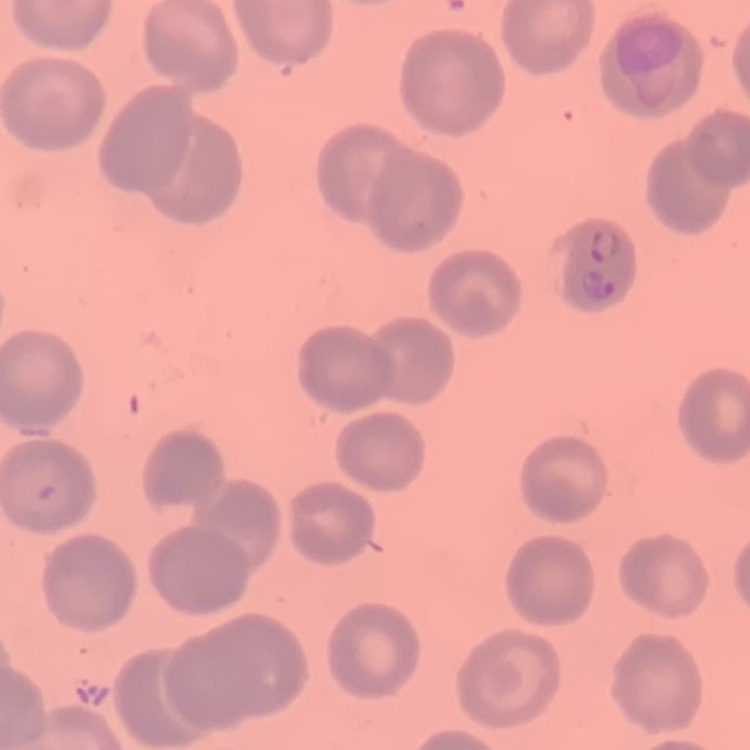

red blood cell morphology = no rouleaux formation
stain = Field's or Giemsa
preparation = thin blood film
image type = one tile cut from a larger photomicrograph